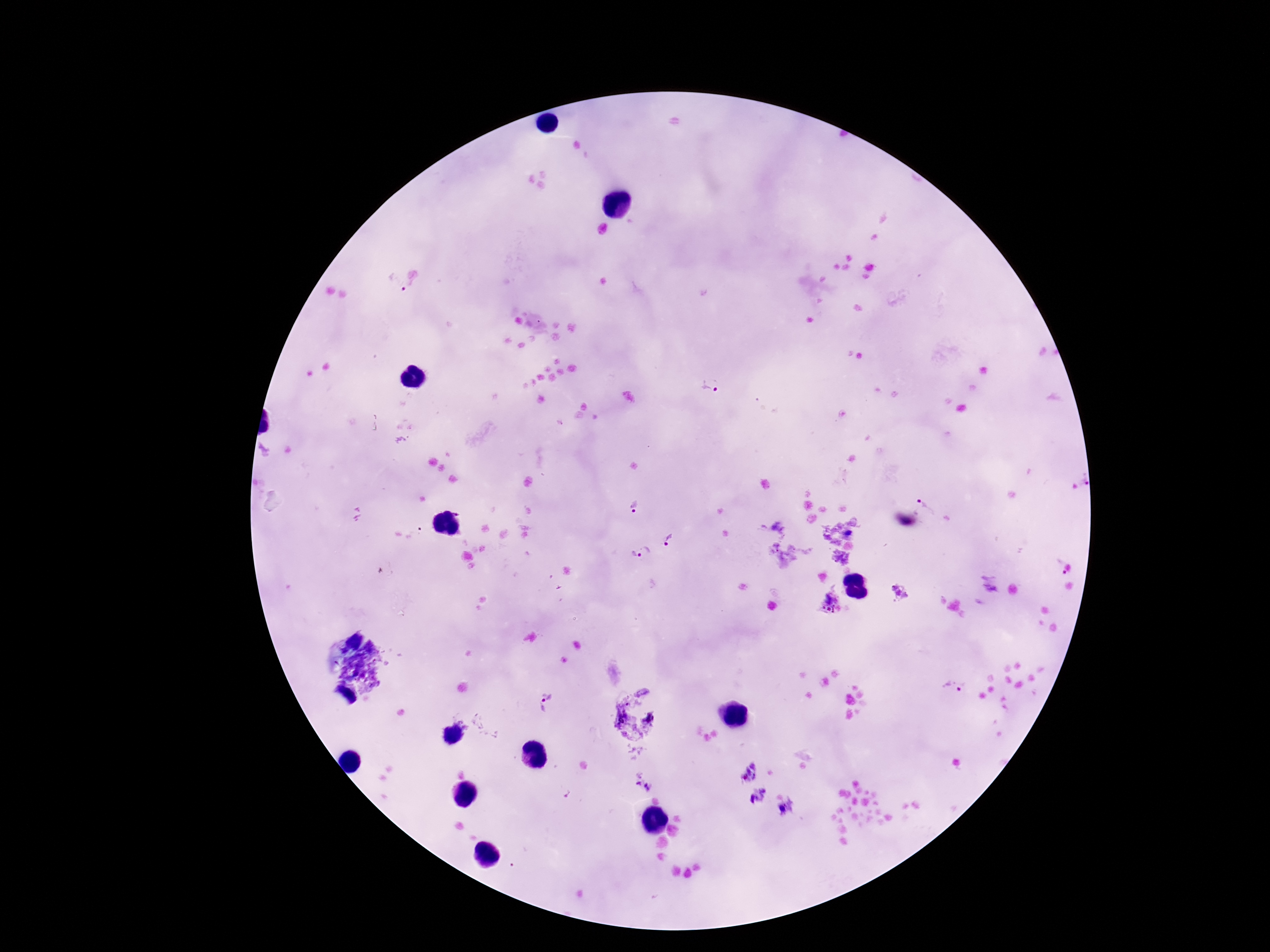
Approximate object centers, in pixels from the top-left corner.
Summary:
  - Plasmodium parasite locations: (x=394, y=284), (x=711, y=384), (x=1083, y=480), (x=927, y=504), (x=633, y=507), (x=670, y=542), (x=641, y=553), (x=1056, y=569), (x=900, y=591), (x=830, y=602), (x=953, y=687), (x=548, y=701), (x=643, y=782)
  - Capture: smartphone camera through the microscope eyepiece
  - Preparation: thick blood smear
  - Field of view: single
  - Image size: 1270×952 pixels
  - Magnification: 100x
  - Stain: Giemsa
  - Patient malaria status: positive